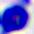
Summary:
  - Magnification: 400x
  - Modality: photomicrograph
  - Identification: leukocyte